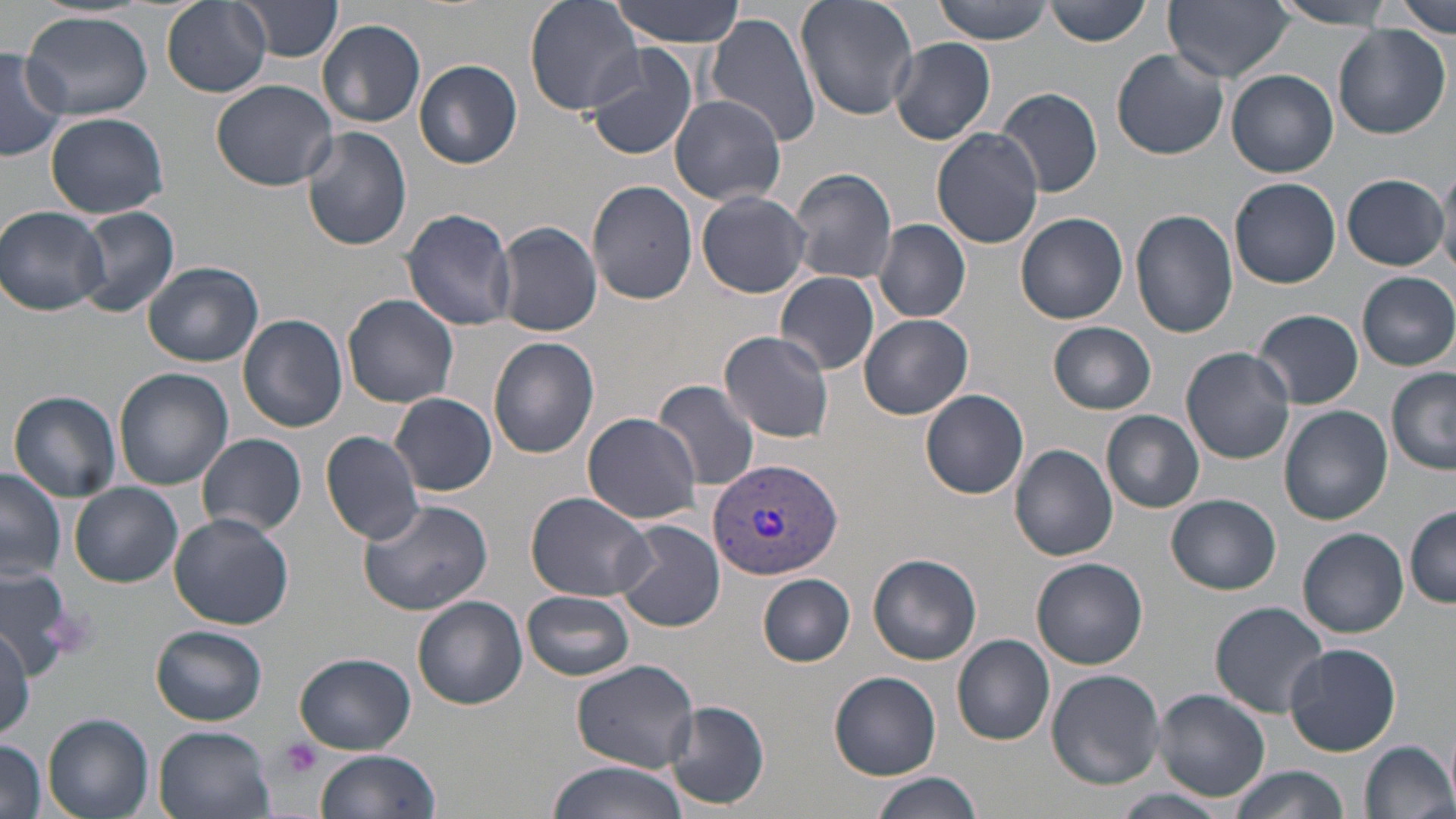
Summary:
  - Coordinate format: approximate bounding boxes as named x1/y1/x2/y2 corners in pixels
  - Uninfected red blood cell locations: (x1=160, y1=0, x2=271, y2=97), (x1=238, y1=0, x2=341, y2=64), (x1=525, y1=0, x2=646, y2=117), (x1=609, y1=0, x2=745, y2=45), (x1=795, y1=0, x2=918, y2=121), (x1=932, y1=0, x2=1056, y2=44), (x1=1044, y1=0, x2=1151, y2=46), (x1=1164, y1=0, x2=1292, y2=82), (x1=1267, y1=1, x2=1395, y2=29), (x1=1388, y1=1, x2=1454, y2=37), (x1=23, y1=11, x2=152, y2=122), (x1=706, y1=11, x2=824, y2=148), (x1=317, y1=19, x2=427, y2=127), (x1=1332, y1=25, x2=1450, y2=141), (x1=889, y1=37, x2=995, y2=144), (x1=582, y1=43, x2=698, y2=162), (x1=0, y1=47, x2=70, y2=161), (x1=1112, y1=50, x2=1229, y2=160), (x1=414, y1=60, x2=523, y2=169), (x1=8, y1=61, x2=104, y2=193), (x1=1227, y1=70, x2=1338, y2=178), (x1=211, y1=78, x2=337, y2=192), (x1=995, y1=86, x2=1104, y2=199), (x1=671, y1=91, x2=789, y2=204), (x1=45, y1=112, x2=168, y2=219), (x1=300, y1=126, x2=413, y2=251), (x1=931, y1=128, x2=1044, y2=248), (x1=1438, y1=162, x2=1456, y2=276), (x1=788, y1=168, x2=898, y2=285), (x1=1341, y1=173, x2=1450, y2=269), (x1=1230, y1=178, x2=1340, y2=288), (x1=587, y1=179, x2=698, y2=304), (x1=696, y1=190, x2=812, y2=298), (x1=0, y1=205, x2=110, y2=316), (x1=77, y1=207, x2=179, y2=319), (x1=400, y1=207, x2=518, y2=330), (x1=1133, y1=208, x2=1239, y2=338), (x1=1016, y1=212, x2=1129, y2=324), (x1=875, y1=219, x2=971, y2=323), (x1=494, y1=221, x2=604, y2=337), (x1=144, y1=260, x2=264, y2=367), (x1=775, y1=272, x2=879, y2=375), (x1=1356, y1=272, x2=1456, y2=371), (x1=343, y1=294, x2=459, y2=408), (x1=1254, y1=309, x2=1363, y2=409), (x1=236, y1=314, x2=349, y2=432), (x1=860, y1=314, x2=974, y2=419), (x1=1046, y1=321, x2=1157, y2=414), (x1=718, y1=331, x2=838, y2=444), (x1=488, y1=336, x2=599, y2=460), (x1=1179, y1=346, x2=1296, y2=463), (x1=1386, y1=367, x2=1456, y2=473), (x1=115, y1=368, x2=233, y2=492), (x1=652, y1=379, x2=763, y2=491), (x1=919, y1=389, x2=1030, y2=500), (x1=9, y1=391, x2=122, y2=503), (x1=390, y1=392, x2=498, y2=496), (x1=1279, y1=406, x2=1392, y2=526), (x1=1101, y1=409, x2=1204, y2=512), (x1=582, y1=412, x2=704, y2=524), (x1=320, y1=429, x2=429, y2=544), (x1=198, y1=432, x2=308, y2=538), (x1=1009, y1=444, x2=1117, y2=562), (x1=1, y1=466, x2=64, y2=584), (x1=71, y1=483, x2=183, y2=587), (x1=526, y1=491, x2=657, y2=602), (x1=1167, y1=494, x2=1281, y2=595), (x1=358, y1=497, x2=494, y2=614), (x1=1405, y1=507, x2=1456, y2=606), (x1=167, y1=510, x2=295, y2=629), (x1=613, y1=519, x2=726, y2=632), (x1=1298, y1=527, x2=1409, y2=638), (x1=867, y1=553, x2=981, y2=666), (x1=1031, y1=557, x2=1148, y2=670), (x1=0, y1=568, x2=80, y2=669), (x1=756, y1=573, x2=856, y2=667), (x1=523, y1=590, x2=634, y2=680), (x1=413, y1=595, x2=527, y2=710), (x1=1209, y1=601, x2=1327, y2=717), (x1=152, y1=626, x2=268, y2=723), (x1=953, y1=634, x2=1056, y2=745), (x1=1284, y1=644, x2=1402, y2=756), (x1=294, y1=654, x2=417, y2=754), (x1=571, y1=659, x2=698, y2=773), (x1=1045, y1=669, x2=1165, y2=789), (x1=830, y1=671, x2=941, y2=779), (x1=1151, y1=688, x2=1271, y2=802), (x1=664, y1=699, x2=769, y2=811), (x1=43, y1=714, x2=156, y2=819), (x1=154, y1=725, x2=276, y2=819), (x1=0, y1=739, x2=48, y2=819), (x1=1359, y1=740, x2=1455, y2=819), (x1=314, y1=750, x2=440, y2=819), (x1=544, y1=761, x2=692, y2=819), (x1=1230, y1=765, x2=1346, y2=819), (x1=868, y1=771, x2=982, y2=819), (x1=1116, y1=790, x2=1227, y2=817)
  - Platelet locations: (x1=276, y1=739, x2=324, y2=779)
  - Plasmodium vivax-infected red blood cell locations: (x1=707, y1=458, x2=845, y2=580)
  - Slide-level diagnosis: Plasmodium vivax
  - Image size: 1456×819 pixels
  - Modality: optical microscopy
  - Preparation: thin blood film
  - Field of view: single
  - Magnification: 1000x
  - Stain: May-Grünwald-Giemsa